Locate and identify every blood parasite.
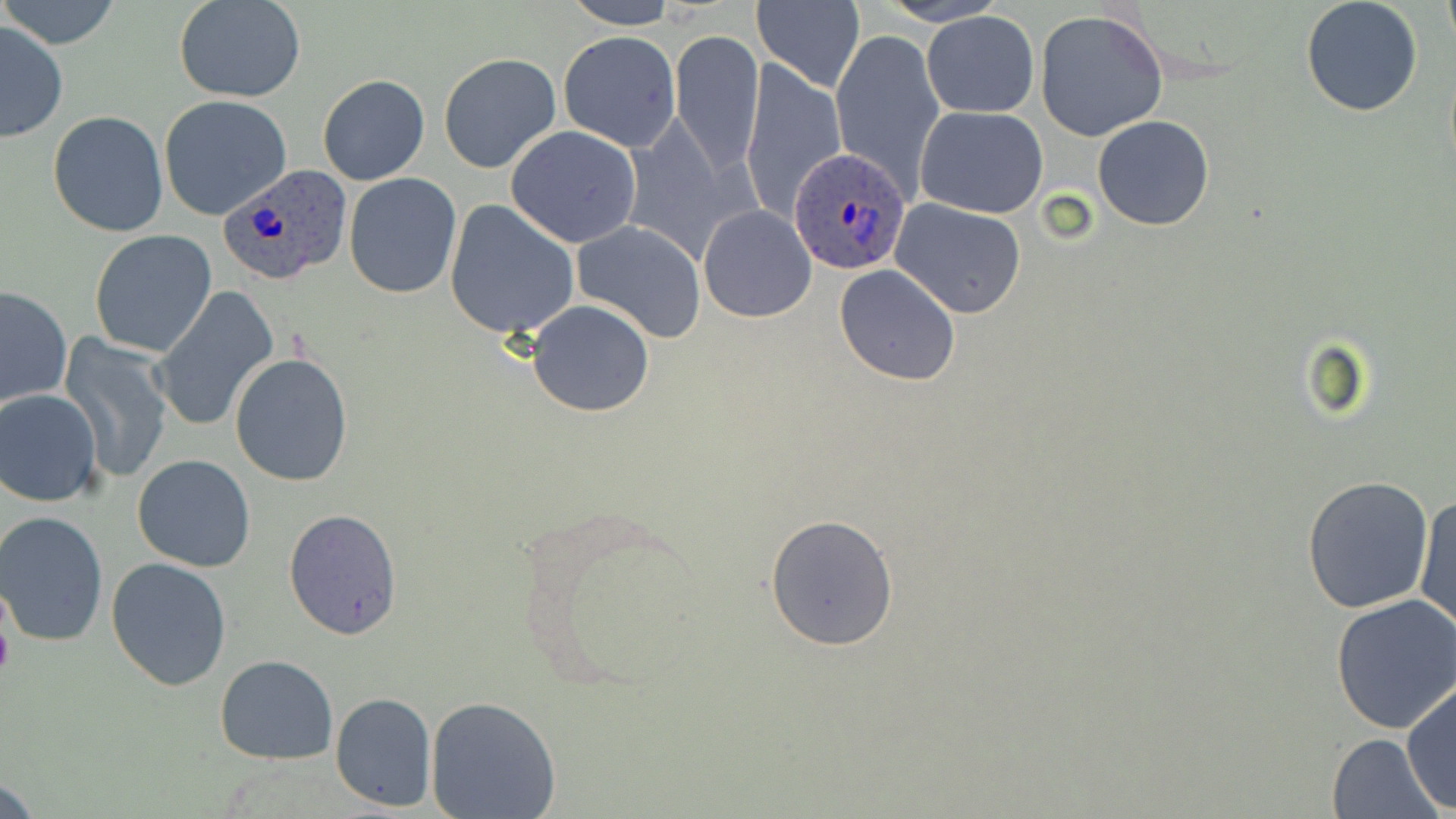

Approximate bounding boxes as (x1,y1)-(x2,y2) corner pairs in pixels.
Plasmodium ovale-infected red blood cells: (790,148)-(911,275), (216,160)-(353,287).
No Plasmodium falciparum, Plasmodium malariae, Plasmodium vivax, Babesia divergens, or Trypanosoma brucei observed.

slide_level_diagnosis: Plasmodium ovale
preparation: thin blood film
stain: May-Grünwald-Giemsa
magnification: 1000x
uninfected_red_blood_cell_locations: 'approximate bounding boxes as (x1,y1)-(x2,y2) corner pairs in pixels: (1,0)-(123,51), (174,0)-(307,102), (876,0)-(1009,26), (1301,0)-(1425,118), (1439,0)-(1454,53), (561,1)-(679,29), (752,1)-(865,93), (1034,8)-(1168,140), (923,11)-(1039,118), (0,21)-(69,141), (829,26)-(943,198), (669,29)-(765,179), (558,30)-(682,151), (437,52)-(561,173), (738,59)-(848,224), (317,73)-(429,186), (159,95)-(293,221), (916,105)-(1048,219), (48,110)-(169,238), (1092,115)-(1214,233), (504,125)-(642,247), (344,172)-(461,298), (890,199)-(1027,318), (443,200)-(582,340), (698,204)-(818,323), (573,220)-(707,343), (89,228)-(218,357), (833,265)-(961,387), (0,285)-(73,409), (148,286)-(280,433), (527,300)-(655,418), (59,333)-(175,485), (228,352)-(354,487), (0,389)-(103,506), (132,454)-(256,571), (1302,474)-(1436,615), (1414,491)-(1454,636), (283,506)-(405,638), (1,512)-(112,648), (764,514)-(899,651), (105,556)-(232,692), (1330,592)-(1456,734), (215,654)-(339,764), (1401,680)-(1455,815), (330,692)-(437,812), (425,696)-(562,818), (1325,732)-(1444,819)'
image_size: 1456×819 pixels
field_of_view: single
modality: light microscopy